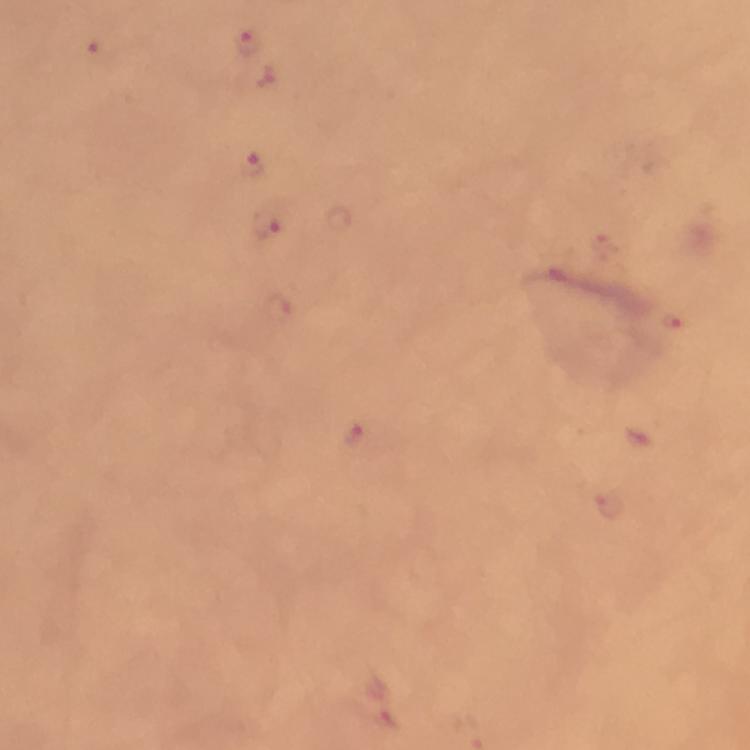

image size = 750×750 pixels
stain = Giemsa
context = from a diagnostic examination for malaria
magnification = 100x
Plasmodium parasite locations = approximate centers as [x, y] in pixels: [247, 41], [100, 55], [268, 80], [252, 164], [271, 223], [279, 312], [672, 322], [354, 437], [606, 506]
cropped from = one field of view
capture = smartphone photograph through a microscope
preparation = thick smear
immersion oil = applied